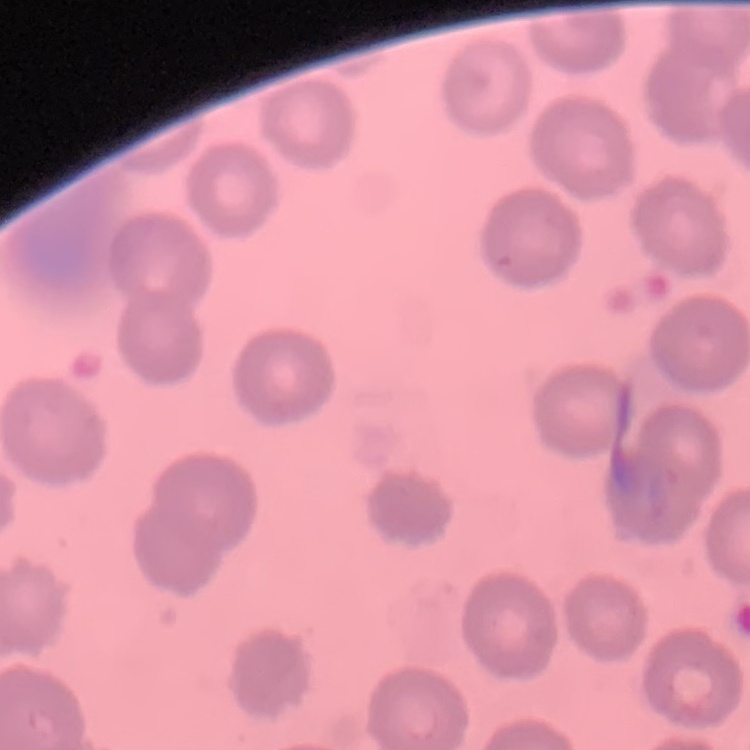

erythrocyte morphology = no rouleaux formation
stain = Field's or Giemsa
image type = one tile cut from a larger photomicrograph
preparation = thin blood smear